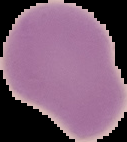
preparation = thin blood smear
image size = 127×142 pixels
image type = segmented cell region on a black background
malaria status = uninfected